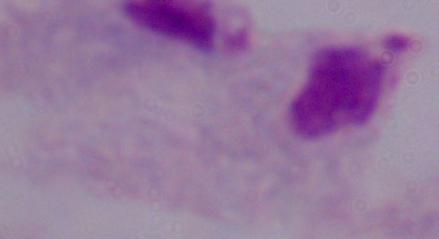
Micrograph. A trichomonad is shown. Captured at 1000x magnification.